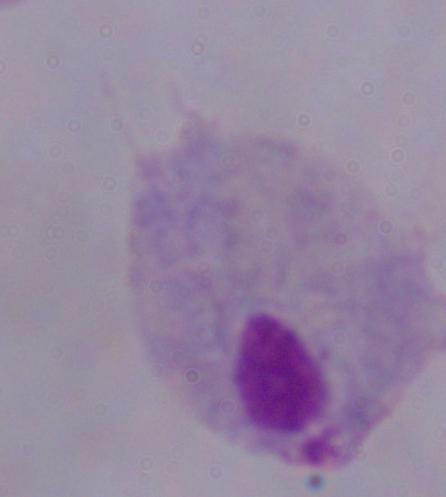
Summary:
  - Magnification: 1000x
  - Identification: trichomonad
  - Modality: photomicrograph